Report the malaria status of this cell.
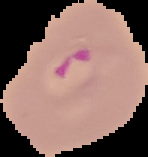
It is parasitized.

Image is 148×157 pixels. Segmented cell region on a black background. From a thin blood smear.